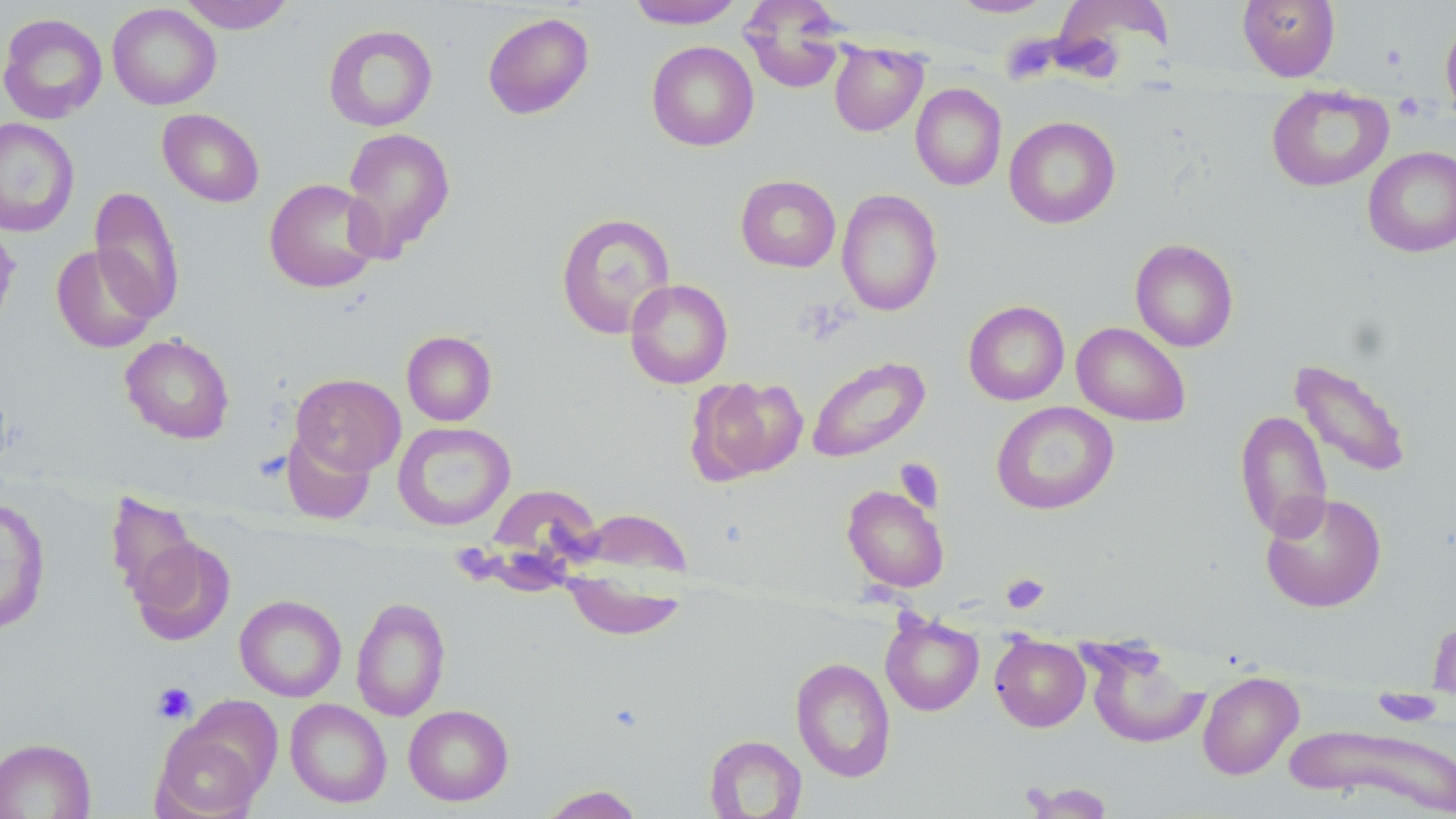

Summary:
  - Coordinate format: approximate bounding boxes as (x1, y1, x2, y2) in pixels
  - Platelet locations: (1393, 92, 1425, 121), (1000, 572, 1050, 614), (152, 682, 197, 724)
  - Uninfected red blood cell locations: (179, 0, 295, 33), (625, 0, 745, 29), (739, 0, 847, 94), (949, 0, 1055, 17), (1049, 0, 1175, 76), (1237, 0, 1340, 82), (107, 4, 221, 110), (482, 12, 594, 119), (0, 13, 107, 124), (1440, 19, 1456, 122), (323, 24, 438, 131), (647, 41, 759, 151), (829, 41, 928, 136), (911, 83, 1007, 191), (1266, 85, 1393, 191), (157, 108, 265, 207), (1004, 116, 1121, 229), (0, 118, 80, 237), (341, 127, 455, 262), (1363, 146, 1456, 257), (735, 174, 841, 273), (264, 177, 382, 293), (89, 185, 185, 322), (836, 189, 943, 317), (555, 212, 676, 339), (0, 222, 21, 341), (1130, 238, 1239, 352), (51, 244, 160, 353), (625, 279, 733, 389), (963, 300, 1069, 405), (1072, 321, 1191, 427), (402, 330, 497, 426), (120, 333, 235, 444), (806, 356, 930, 463), (1288, 358, 1413, 479), (291, 373, 405, 476), (688, 375, 808, 484), (991, 401, 1119, 515), (1235, 409, 1332, 541), (393, 422, 515, 531), (280, 429, 376, 526), (842, 484, 950, 593), (473, 489, 595, 603), (105, 491, 200, 604), (1260, 491, 1387, 612), (0, 498, 51, 633), (563, 508, 692, 634), (130, 537, 236, 645), (234, 595, 347, 701), (351, 596, 451, 721), (1428, 610, 1456, 704), (880, 615, 984, 717), (990, 636, 1090, 732), (1084, 641, 1208, 749), (790, 657, 896, 782), (1197, 671, 1303, 780), (285, 699, 392, 808), (403, 704, 514, 806), (152, 723, 267, 819), (1284, 723, 1456, 814), (704, 734, 807, 819), (0, 737, 96, 818), (540, 785, 644, 819)
  - Slide-level diagnosis: negative for blood parasites
  - Field of view: one of a larger specimen
  - Preparation: thin blood film
  - Modality: optical microscopy
  - Magnification: 1000x
  - Image size: 1456×819 pixels
  - Stain: May-Grünwald-Giemsa